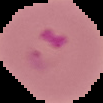

image type = cell region segmented out of the field of view; surrounding area masked to black
preparation = thin blood smear
malaria status = parasitized
image size = 103×103 pixels